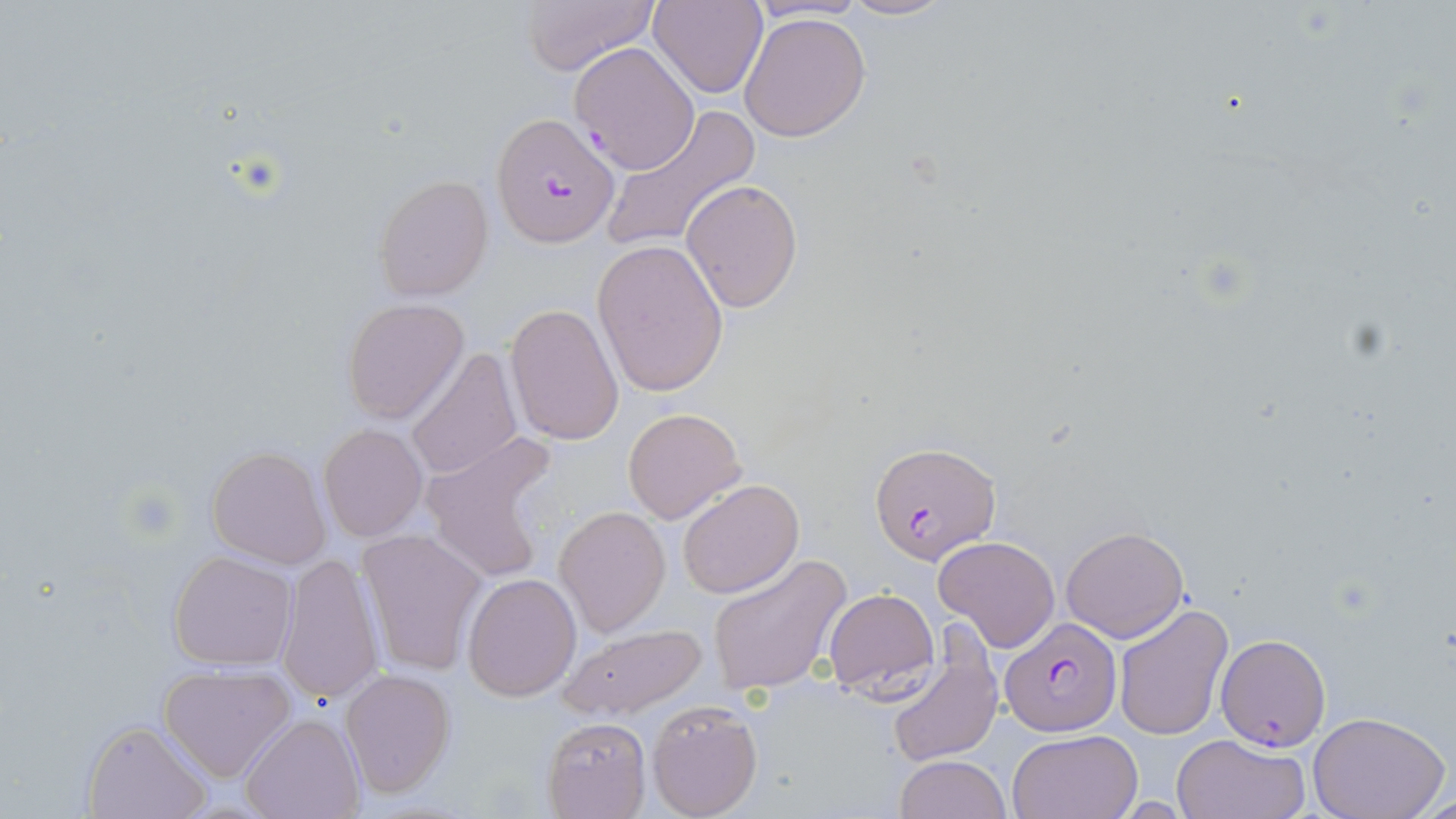

Summary:
  - Coordinate format: approximate bounding boxes as (x1, y1, x2, y2) in pixels
  - Plasmodium falciparum-infected red blood cell locations: (571, 38, 699, 172), (493, 112, 619, 248), (870, 440, 1001, 564), (1000, 617, 1121, 736), (1216, 632, 1333, 751)
  - Uninfected red blood cell locations: (518, 0, 657, 76), (650, 0, 767, 98), (839, 0, 956, 22), (738, 10, 872, 143), (598, 107, 759, 256), (372, 174, 494, 301), (680, 179, 803, 313), (591, 237, 731, 397), (341, 298, 469, 424), (505, 302, 623, 445), (407, 349, 524, 483), (621, 408, 745, 523), (319, 423, 428, 541), (421, 432, 561, 583), (206, 446, 333, 569), (676, 478, 804, 599), (553, 506, 671, 636), (1060, 526, 1189, 643), (355, 528, 489, 679), (934, 534, 1060, 651), (168, 551, 297, 671), (705, 554, 851, 696), (275, 555, 385, 705), (461, 571, 581, 702), (821, 588, 940, 699), (1114, 603, 1233, 742), (555, 621, 708, 721), (884, 641, 1003, 767), (156, 662, 297, 781), (339, 668, 455, 798), (646, 700, 763, 817), (1308, 712, 1450, 819), (240, 714, 362, 819), (542, 716, 650, 818), (81, 719, 211, 819), (1007, 730, 1142, 818), (1171, 732, 1311, 819), (894, 755, 1012, 818)
  - Slide-level diagnosis: Plasmodium falciparum
  - Modality: optical microscopy
  - Magnification: 1000x
  - Preparation: thin blood smear
  - Field of view: single
  - Stain: May-Grünwald-Giemsa
  - Image size: 1456×819 pixels